Classify this cell by malaria status.
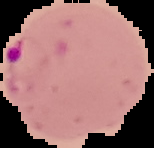

Parasitized.

Image is 154×148 pixels. From a thin blood film. Cell region segmented out of the field of view; the surrounding area is masked to black.